Classify this cell by malaria status.
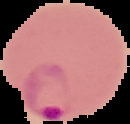
Parasitized.

Cell region segmented out of the field of view; the surrounding area is masked to black. From a thin blood smear. Image is 130×124 pixels.